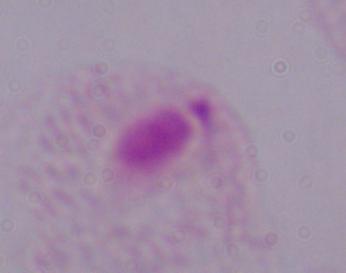 A trichomonad is shown. Photomicrograph. 1000x magnification.